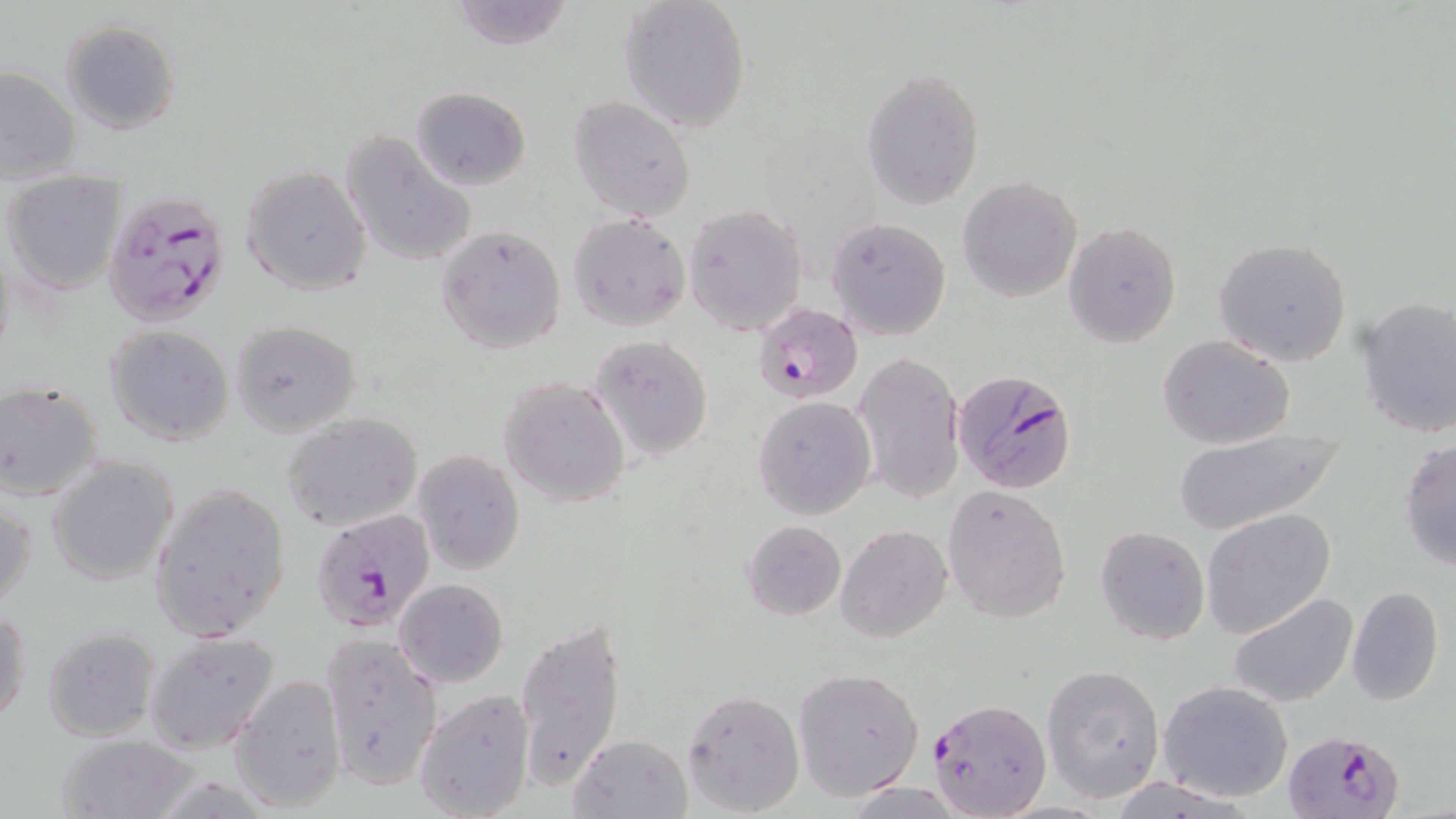

slide-level diagnosis = Plasmodium falciparum
magnification = 1000x
stain = May-Grünwald-Giemsa
Plasmodium falciparum-infected red blood cell locations = approximate bounding boxes as [x1, y1, x2, y2] in pixels: [104, 188, 233, 330], [755, 301, 862, 403], [951, 368, 1078, 494], [310, 507, 436, 632], [925, 698, 1051, 818], [1281, 730, 1403, 819]
image size = 1456×819 pixels
uninfected red blood cell locations = approximate bounding boxes as [x1, y1, x2, y2] in pixels: [444, 0, 575, 50], [618, 0, 753, 133], [60, 19, 181, 134], [0, 65, 80, 182], [861, 66, 983, 207], [411, 87, 531, 191], [570, 96, 695, 220], [341, 130, 478, 268], [241, 165, 372, 297], [4, 171, 127, 295], [958, 175, 1083, 303], [685, 204, 809, 336], [567, 213, 690, 331], [827, 217, 952, 340], [1063, 222, 1181, 348], [435, 226, 567, 354], [1211, 237, 1355, 367], [1355, 296, 1456, 438], [230, 319, 362, 436], [105, 325, 235, 444], [589, 334, 715, 461], [1156, 335, 1295, 450], [854, 349, 967, 506], [498, 377, 633, 506], [0, 382, 105, 501], [752, 395, 876, 519], [282, 413, 423, 531], [1170, 429, 1348, 535], [1398, 438, 1455, 571], [412, 450, 525, 574], [47, 455, 182, 586], [150, 483, 291, 646], [942, 484, 1072, 624], [1, 491, 37, 613], [1201, 510, 1335, 639], [742, 520, 846, 620], [837, 525, 952, 644], [1094, 525, 1210, 645], [394, 578, 508, 689], [1345, 585, 1444, 705], [1229, 592, 1358, 707], [1, 606, 30, 729], [515, 617, 627, 792], [41, 627, 160, 742], [145, 632, 279, 754], [320, 633, 442, 791], [1042, 665, 1165, 801], [793, 667, 925, 800], [228, 676, 347, 811], [1157, 680, 1293, 802], [413, 688, 536, 819], [681, 688, 804, 816], [568, 733, 693, 818], [56, 735, 200, 819]
preparation = thin blood smear
field of view = one of a larger specimen
modality = light microscopy